Assess the morphology of the erythrocytes.
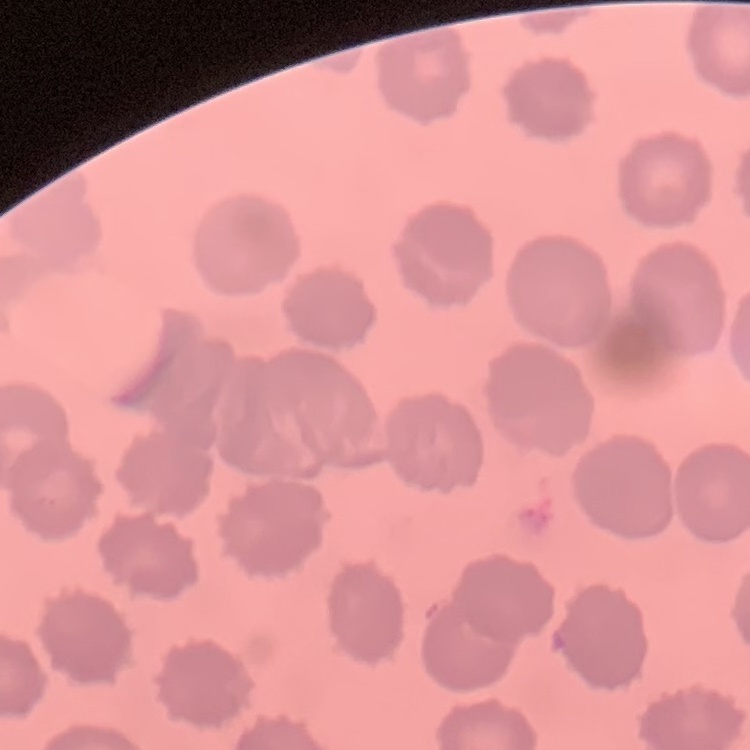
They show no rouleaux formation.

One tile cut from a larger photomicrograph. Thin blood smear. Field's or Giemsa stain.